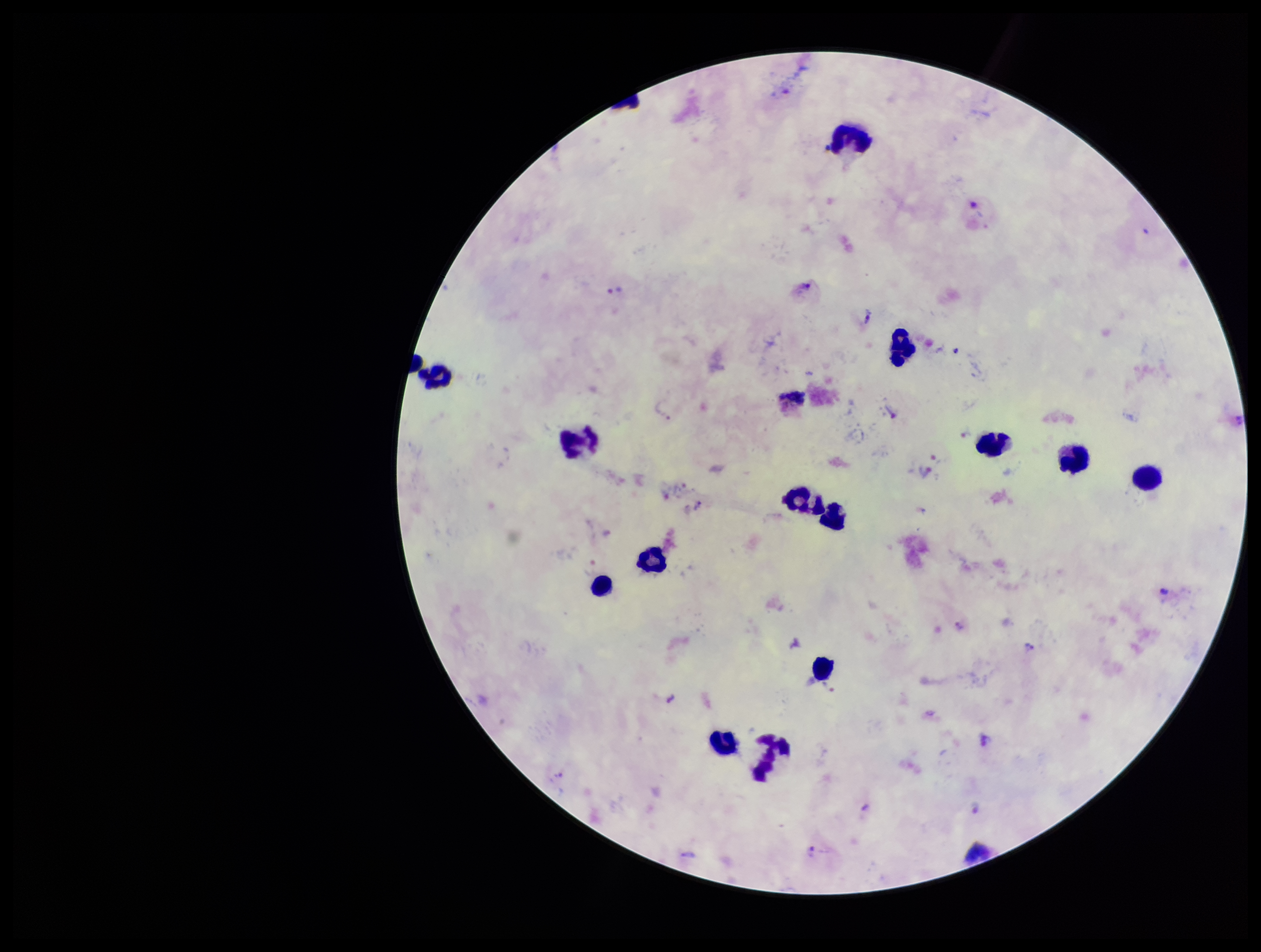

Summary:
  - Patient malaria status: infected
  - Image size: 1261×952 pixels
  - Field of view: one from this slide
  - Preparation: thick smear
  - Parasite count: 13
  - Capture: smartphone photograph through the microscope eyepiece
  - Species reported for this patient: Plasmodium vivax
  - Stain: Giemsa
  - Plasmodium parasites: detected
  - Leukocyte count: 15